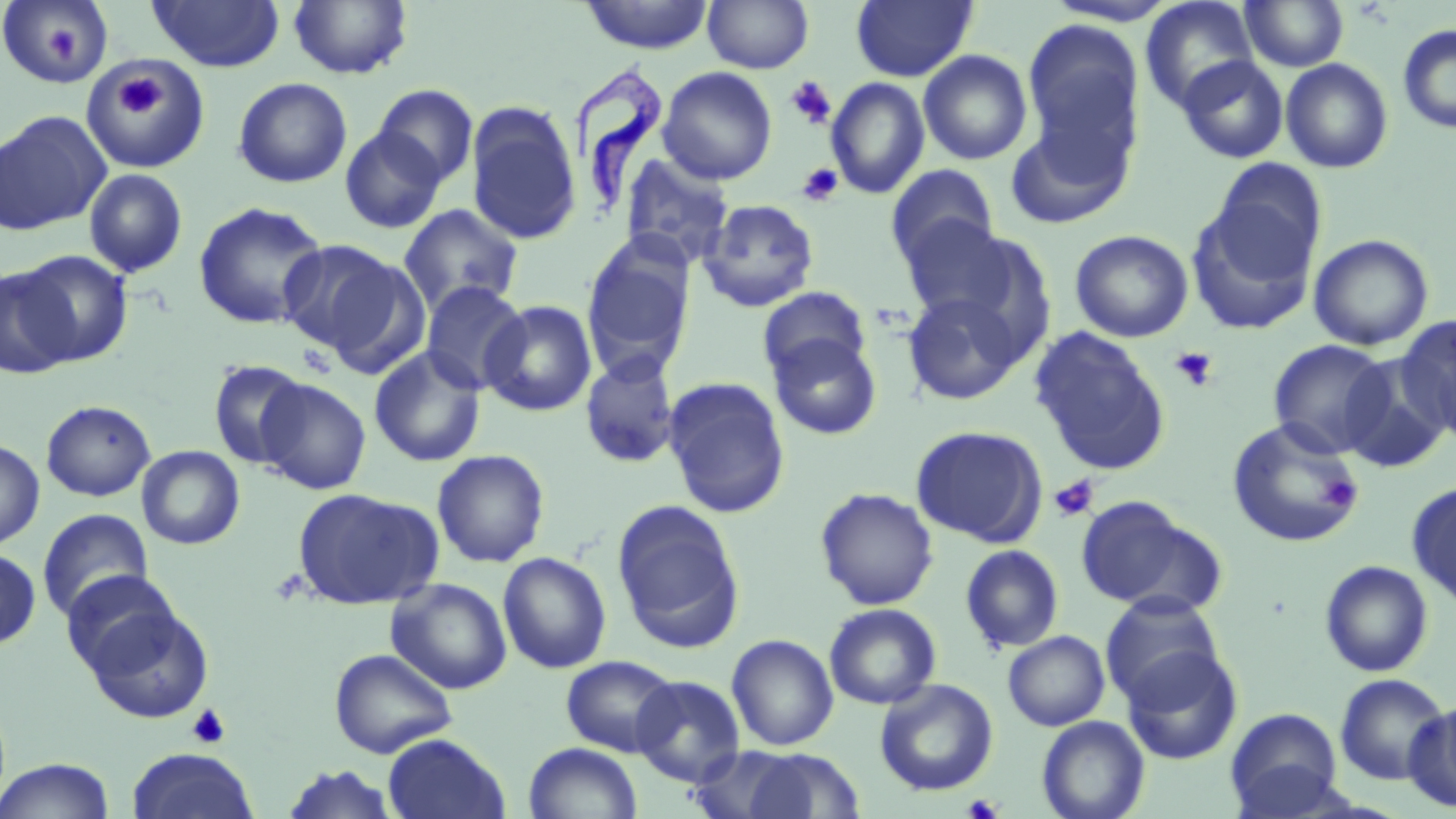
{
  "slide_level_diagnosis": "Trypanosoma brucei",
  "platelet_locations": "approximate bounding boxes as named x1/y1/x2/y2 corners in pixels: (x1=47, y1=27, x2=79, y2=65), (x1=113, y1=75, x2=166, y2=119), (x1=785, y1=76, x2=837, y2=129), (x1=797, y1=162, x2=843, y2=206), (x1=1169, y1=346, x2=1218, y2=391), (x1=1049, y1=475, x2=1099, y2=522), (x1=1320, y1=475, x2=1361, y2=512), (x1=186, y1=704, x2=231, y2=750), (x1=962, y1=793, x2=1005, y2=819)",
  "magnification": "1000x",
  "uninfected_red_blood_cell_locations": "approximate bounding boxes as named x1/y1/x2/y2 corners in pixels: (x1=147, y1=0, x2=285, y2=71), (x1=289, y1=0, x2=413, y2=80), (x1=578, y1=0, x2=714, y2=54), (x1=702, y1=0, x2=814, y2=73), (x1=851, y1=0, x2=977, y2=82), (x1=1042, y1=0, x2=1181, y2=26), (x1=1140, y1=0, x2=1260, y2=113), (x1=1240, y1=0, x2=1349, y2=71), (x1=0, y1=1, x2=113, y2=89), (x1=1021, y1=18, x2=1145, y2=167), (x1=1397, y1=24, x2=1456, y2=134), (x1=918, y1=49, x2=1033, y2=165), (x1=86, y1=55, x2=205, y2=168), (x1=1177, y1=55, x2=1288, y2=163), (x1=1280, y1=58, x2=1393, y2=173), (x1=658, y1=66, x2=778, y2=185), (x1=233, y1=77, x2=353, y2=188), (x1=826, y1=77, x2=930, y2=199), (x1=372, y1=84, x2=479, y2=189), (x1=465, y1=104, x2=582, y2=245), (x1=0, y1=111, x2=110, y2=235), (x1=1004, y1=115, x2=1134, y2=230), (x1=340, y1=126, x2=447, y2=234), (x1=618, y1=152, x2=736, y2=270), (x1=1208, y1=159, x2=1327, y2=280), (x1=886, y1=164, x2=999, y2=268), (x1=84, y1=169, x2=188, y2=278), (x1=1185, y1=197, x2=1319, y2=336), (x1=698, y1=198, x2=819, y2=313), (x1=193, y1=201, x2=329, y2=330), (x1=398, y1=204, x2=524, y2=316), (x1=897, y1=216, x2=1022, y2=326), (x1=919, y1=226, x2=1060, y2=365), (x1=1069, y1=229, x2=1194, y2=342), (x1=1308, y1=234, x2=1434, y2=351), (x1=581, y1=236, x2=696, y2=380), (x1=276, y1=240, x2=403, y2=357), (x1=19, y1=250, x2=132, y2=366), (x1=316, y1=251, x2=432, y2=381), (x1=0, y1=266, x2=76, y2=379), (x1=420, y1=280, x2=530, y2=395), (x1=758, y1=285, x2=871, y2=384), (x1=902, y1=291, x2=1028, y2=406), (x1=482, y1=300, x2=597, y2=417), (x1=1394, y1=315, x2=1456, y2=439), (x1=1029, y1=327, x2=1170, y2=475), (x1=767, y1=332, x2=883, y2=440), (x1=1268, y1=339, x2=1393, y2=457), (x1=369, y1=346, x2=486, y2=467), (x1=1339, y1=352, x2=1453, y2=474), (x1=580, y1=354, x2=680, y2=469), (x1=207, y1=359, x2=311, y2=469), (x1=662, y1=376, x2=792, y2=519), (x1=255, y1=378, x2=371, y2=495), (x1=41, y1=400, x2=156, y2=501), (x1=1226, y1=417, x2=1365, y2=549), (x1=911, y1=425, x2=1047, y2=547), (x1=0, y1=438, x2=44, y2=549), (x1=137, y1=445, x2=245, y2=549), (x1=431, y1=449, x2=550, y2=568), (x1=1408, y1=481, x2=1456, y2=611), (x1=292, y1=487, x2=443, y2=610), (x1=815, y1=487, x2=939, y2=610), (x1=1075, y1=496, x2=1221, y2=614), (x1=611, y1=500, x2=745, y2=651), (x1=37, y1=509, x2=154, y2=623), (x1=960, y1=544, x2=1064, y2=654), (x1=0, y1=548, x2=41, y2=650), (x1=497, y1=551, x2=612, y2=673), (x1=1319, y1=560, x2=1434, y2=677), (x1=60, y1=569, x2=182, y2=674), (x1=386, y1=577, x2=513, y2=694), (x1=1099, y1=592, x2=1226, y2=708), (x1=84, y1=603, x2=214, y2=724), (x1=824, y1=603, x2=942, y2=709), (x1=1003, y1=630, x2=1110, y2=731), (x1=726, y1=633, x2=838, y2=750), (x1=1120, y1=646, x2=1243, y2=764), (x1=329, y1=648, x2=457, y2=758), (x1=561, y1=654, x2=680, y2=757), (x1=1334, y1=674, x2=1451, y2=786), (x1=630, y1=675, x2=746, y2=787), (x1=875, y1=679, x2=998, y2=797), (x1=1404, y1=700, x2=1456, y2=814), (x1=1224, y1=707, x2=1346, y2=818), (x1=1036, y1=716, x2=1150, y2=819), (x1=383, y1=733, x2=510, y2=818), (x1=523, y1=742, x2=643, y2=819), (x1=685, y1=745, x2=814, y2=818), (x1=739, y1=747, x2=864, y2=818), (x1=125, y1=748, x2=259, y2=819), (x1=0, y1=757, x2=116, y2=819), (x1=280, y1=764, x2=400, y2=818)",
  "modality": "optical microscopy",
  "stain": "May-Grünwald-Giemsa",
  "image_size": "1456×819 pixels",
  "preparation": "thin blood film",
  "field_of_view": "single",
  "trypanosoma_brucei_locations": "approximate bounding boxes as named x1/y1/x2/y2 corners in pixels: (x1=567, y1=66, x2=672, y2=225)"
}